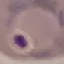
Malaria status: parasitized. Giemsa-stained preparation. Cell patch, automatically extracted from a larger field of view and resized to 64 × 64 pixels. Thin blood film. Photographed with a smartphone camera at the microscope eyepiece.